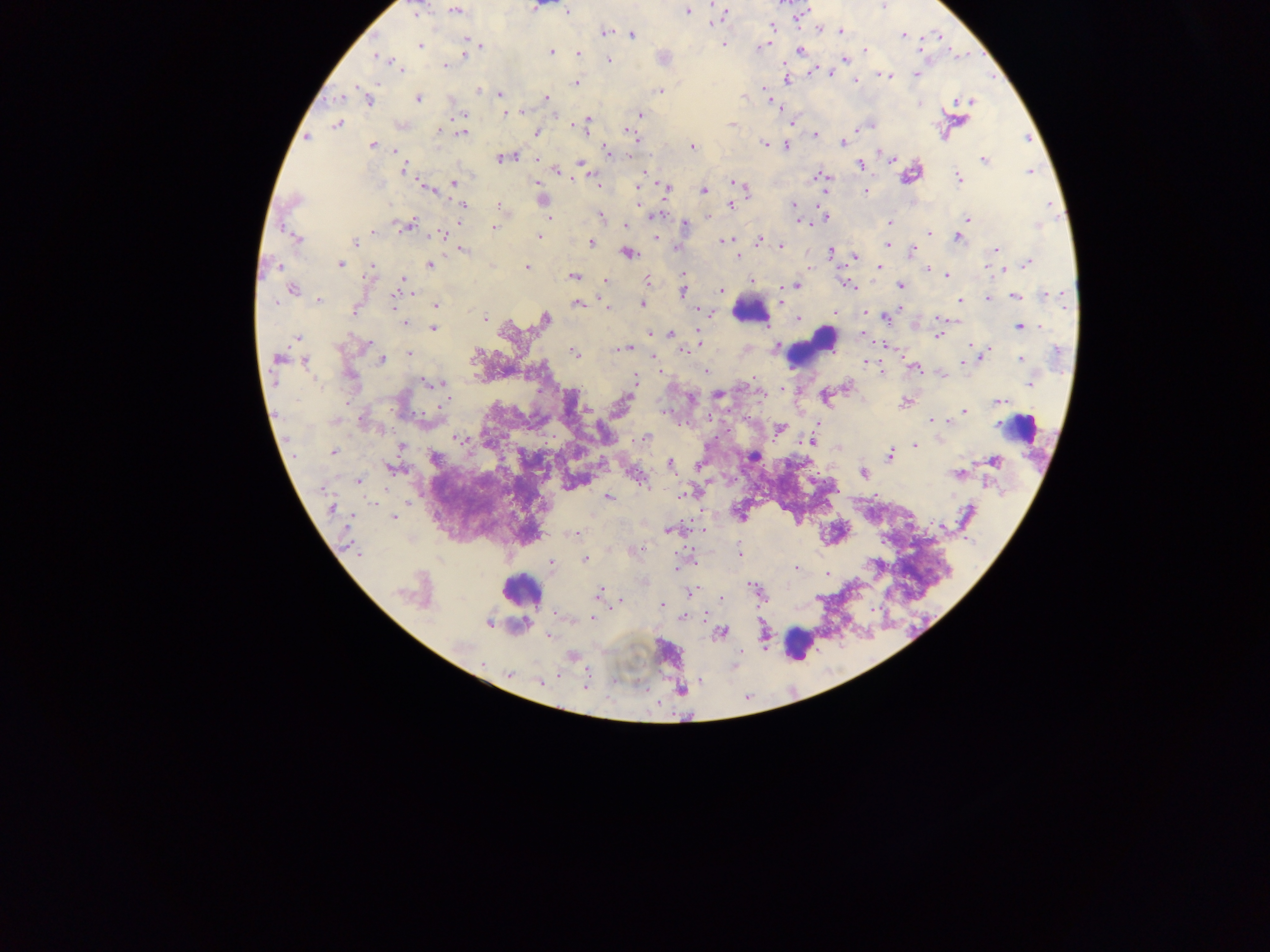

malaria parasite locations = approximate centers as {x, y} in pixels: {884, 5}, {536, 6}, {454, 10}, {685, 10}, {415, 11}, {566, 11}, {724, 13}, {800, 15}, {717, 18}, {713, 22}, {772, 27}, {819, 28}, {840, 31}, {604, 33}, {631, 34}, {938, 35}, {903, 36}, {466, 40}, {723, 43}, {765, 44}, {420, 45}, {481, 46}, {919, 48}, {465, 50}, {799, 50}, {864, 50}, {551, 51}, {578, 53}, {379, 58}, {608, 60}, {844, 60}, {393, 64}, {445, 66}, {398, 67}, {810, 70}, {828, 72}, {883, 74}, {916, 74}, {787, 79}, {854, 82}, {575, 83}, {659, 90}, {479, 91}, {766, 91}, {500, 93}, {767, 96}, {339, 97}, {367, 98}, {418, 98}, {546, 98}, {969, 100}, {775, 104}, {503, 113}, {462, 114}, {638, 114}, {585, 122}, {790, 122}, {337, 124}, {732, 124}, {400, 125}, {440, 131}, {462, 132}, {536, 133}, {815, 134}, {306, 137}, {635, 137}, {843, 143}, {764, 144}, {372, 145}, {787, 145}, {693, 147}, {395, 151}, {606, 152}, {502, 158}, {536, 159}, {891, 160}, {984, 160}, {581, 162}, {859, 164}, {583, 167}, {404, 168}, {1028, 169}, {555, 170}, {645, 174}, {823, 177}, {958, 178}, {454, 183}, {538, 183}, {738, 184}, {597, 186}, {638, 186}, {427, 187}, {665, 188}, {703, 190}, {866, 191}, {542, 200}, {639, 200}, {732, 203}, {463, 205}, {793, 205}, {498, 206}, {796, 211}, {600, 216}, {654, 216}, {708, 216}, {826, 217}, {550, 218}, {967, 218}, {798, 220}, {888, 222}, {685, 224}, {408, 225}, {624, 225}, {493, 228}, {373, 231}, {929, 233}, {442, 234}, {539, 236}, {655, 236}, {957, 237}, {297, 239}, {759, 239}, {725, 241}, {355, 242}, {590, 242}, {887, 244}, {781, 245}, {460, 249}, {994, 249}, {678, 250}, {912, 251}, {626, 252}, {830, 252}, {739, 255}, {854, 256}, {1027, 262}, {339, 263}, {429, 264}, {526, 267}, {877, 267}, {926, 268}, {1003, 268}, {371, 271}, {684, 274}, {947, 275}, {574, 276}, {606, 281}, {647, 281}, {402, 282}, {751, 282}, {796, 285}, {900, 285}, {852, 287}, {291, 289}, {721, 290}, {783, 290}, {682, 291}, {1015, 295}, {1044, 295}, {987, 297}, {318, 300}, {960, 300}, {394, 301}, {780, 302}, {578, 303}, {436, 304}, {641, 304}, {605, 307}, {900, 307}, {354, 308}, {697, 309}, {710, 312}, {835, 313}, {865, 314}, {885, 317}, {485, 318}, {544, 319}, {798, 319}, {941, 319}, {405, 323}, {1020, 327}, {432, 328}, {862, 333}, {671, 334}, {937, 336}, {297, 337}, {700, 343}, {365, 345}, {884, 345}, {971, 345}, {628, 346}, {776, 347}, {684, 351}, {409, 353}, {574, 353}, {653, 353}, {982, 354}, {279, 358}, {1020, 359}, {304, 360}, {382, 361}, {866, 361}, {965, 361}, {915, 367}, {660, 369}, {881, 370}, {706, 371}, {425, 381}, {434, 382}, {1029, 382}, {633, 383}, {847, 387}, {782, 389}, {718, 394}, {691, 398}, {905, 402}, {997, 402}, {586, 410}, {964, 411}, {709, 416}, {361, 419}, {932, 420}, {817, 426}, {779, 428}, {458, 437}, {644, 437}, {812, 441}, {400, 446}, {914, 446}, {839, 447}, {334, 451}, {753, 455}, {889, 455}, {434, 458}, {995, 460}, {671, 462}, {393, 468}, {862, 473}, {958, 473}, {637, 475}, {359, 481}, {681, 495}, {607, 497}, {332, 508}, {392, 518}, {941, 526}, {668, 530}, {574, 533}, {634, 550}, {739, 553}, {584, 560}, {551, 562}, {676, 567}, {796, 567}, {828, 575}, {689, 592}, {599, 593}, {720, 599}, {620, 600}, {662, 605}, {556, 615}, {592, 617}, {683, 617}, {487, 623}, {721, 632}, {549, 635}, {571, 656}, {509, 675}, {541, 683}, {584, 684}
country = Ghana
image size = 1270×952 pixels
field of view = single
preparation = thick blood film
capture = mobile-phone photograph through a microscope
leukocyte locations = approximate centers as {x, y} in pixels: {751, 310}, {814, 344}, {1022, 429}, {521, 589}, {799, 645}